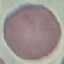

Result: no malaria parasites seen. Giemsa stain. Photographed with a smartphone camera at the microscope eyepiece. Automatically extracted cell patch, resized to 64 × 64 pixels. Thin blood smear.